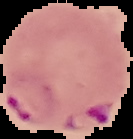

{
  "result": "malaria parasites detected",
  "image_type": "segmented cell region on a black background",
  "image_size": "133×139 pixels",
  "preparation": "thin blood smear"
}